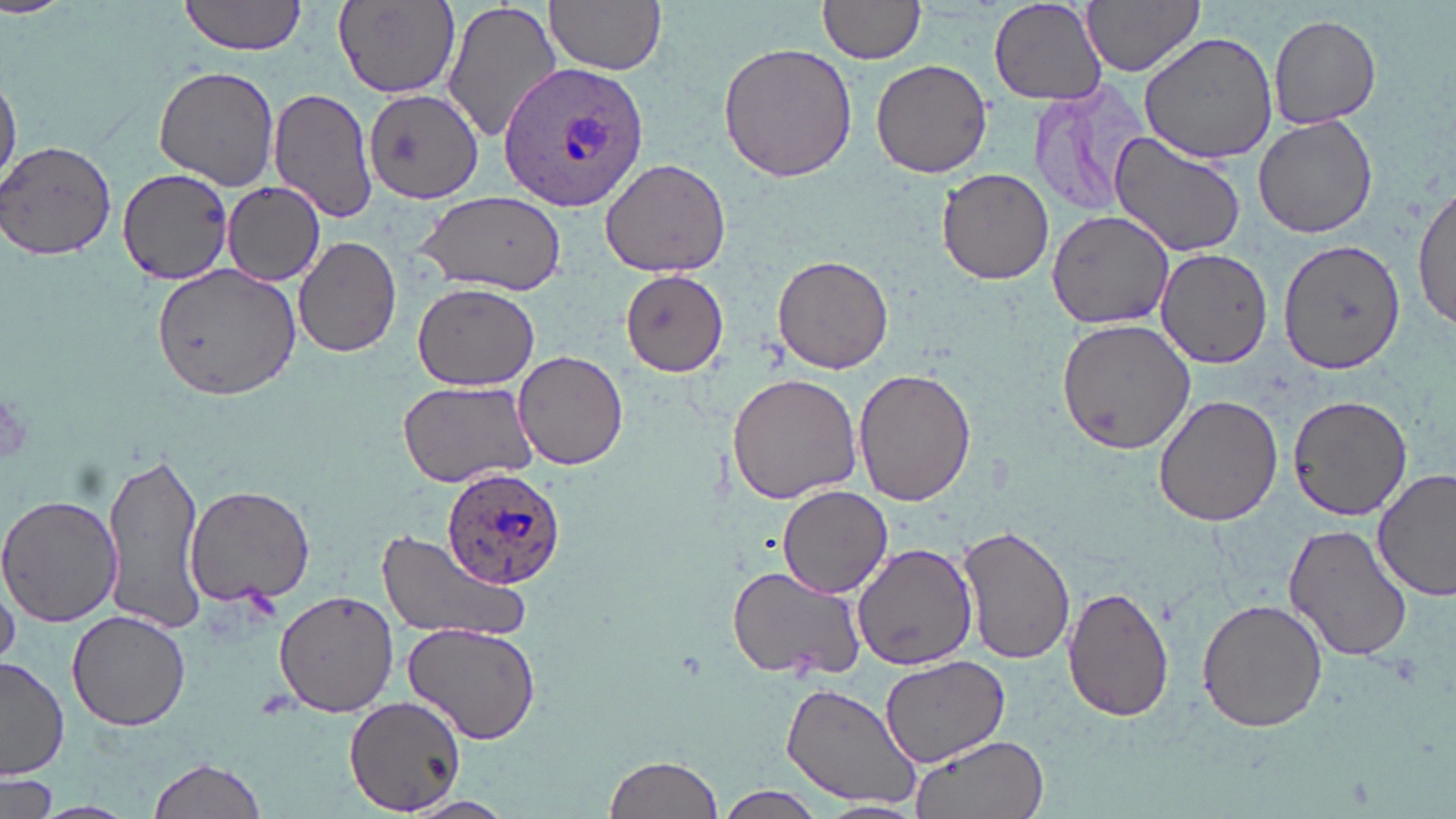
Approximate bounding boxes as [x1, y1, x2, y2] in pixels. Plasmodium ovale-infected red blood cell locations: [497, 63, 651, 208], [442, 468, 566, 589]. Platelet locations: [0, 390, 36, 468]. Uninfected red blood cell locations: [180, 0, 308, 56], [440, 0, 564, 146], [546, 0, 667, 74], [817, 0, 926, 65], [1081, 0, 1204, 79], [989, 1, 1106, 108], [333, 2, 459, 100], [1268, 13, 1381, 129], [1140, 29, 1281, 163], [718, 41, 859, 184], [871, 60, 992, 178], [153, 65, 280, 190], [0, 71, 20, 190], [1025, 81, 1147, 219], [268, 86, 379, 226], [363, 86, 484, 204], [1253, 115, 1379, 239], [1108, 132, 1246, 259], [1, 141, 117, 262], [598, 156, 733, 277], [116, 168, 232, 285], [936, 169, 1055, 284], [223, 185, 325, 288], [1413, 186, 1456, 333], [416, 191, 566, 293], [1046, 209, 1177, 330], [293, 236, 401, 357], [1280, 239, 1405, 374], [1156, 249, 1273, 368], [773, 253, 893, 374], [150, 262, 304, 399], [619, 268, 732, 378], [412, 284, 539, 390], [1056, 317, 1197, 455], [513, 352, 628, 470], [854, 368, 977, 507], [727, 372, 865, 505], [397, 378, 541, 489], [1153, 393, 1283, 528], [1287, 393, 1412, 520], [102, 451, 207, 635], [1375, 467, 1455, 601], [185, 483, 314, 608], [777, 486, 892, 599], [0, 495, 121, 628], [1283, 523, 1411, 663], [957, 525, 1075, 666], [375, 529, 530, 645], [852, 541, 977, 671], [725, 564, 867, 681], [1, 565, 21, 669], [1063, 584, 1176, 722], [273, 590, 398, 717], [1197, 597, 1328, 733], [67, 610, 191, 731], [403, 623, 542, 747], [876, 652, 1009, 768], [1, 656, 70, 781], [782, 681, 924, 811], [345, 697, 466, 815], [910, 734, 1049, 819], [603, 752, 726, 819], [146, 755, 269, 819], [0, 774, 58, 819], [715, 786, 825, 819], [400, 798, 515, 819], [27, 800, 140, 819], [810, 800, 930, 819]. Slide-level diagnosis: Plasmodium ovale. Thin blood film. Light microscopy. Image is 1456×819 pixels. 1000x magnification. Single field of view. May-Grünwald-Giemsa-stained preparation.